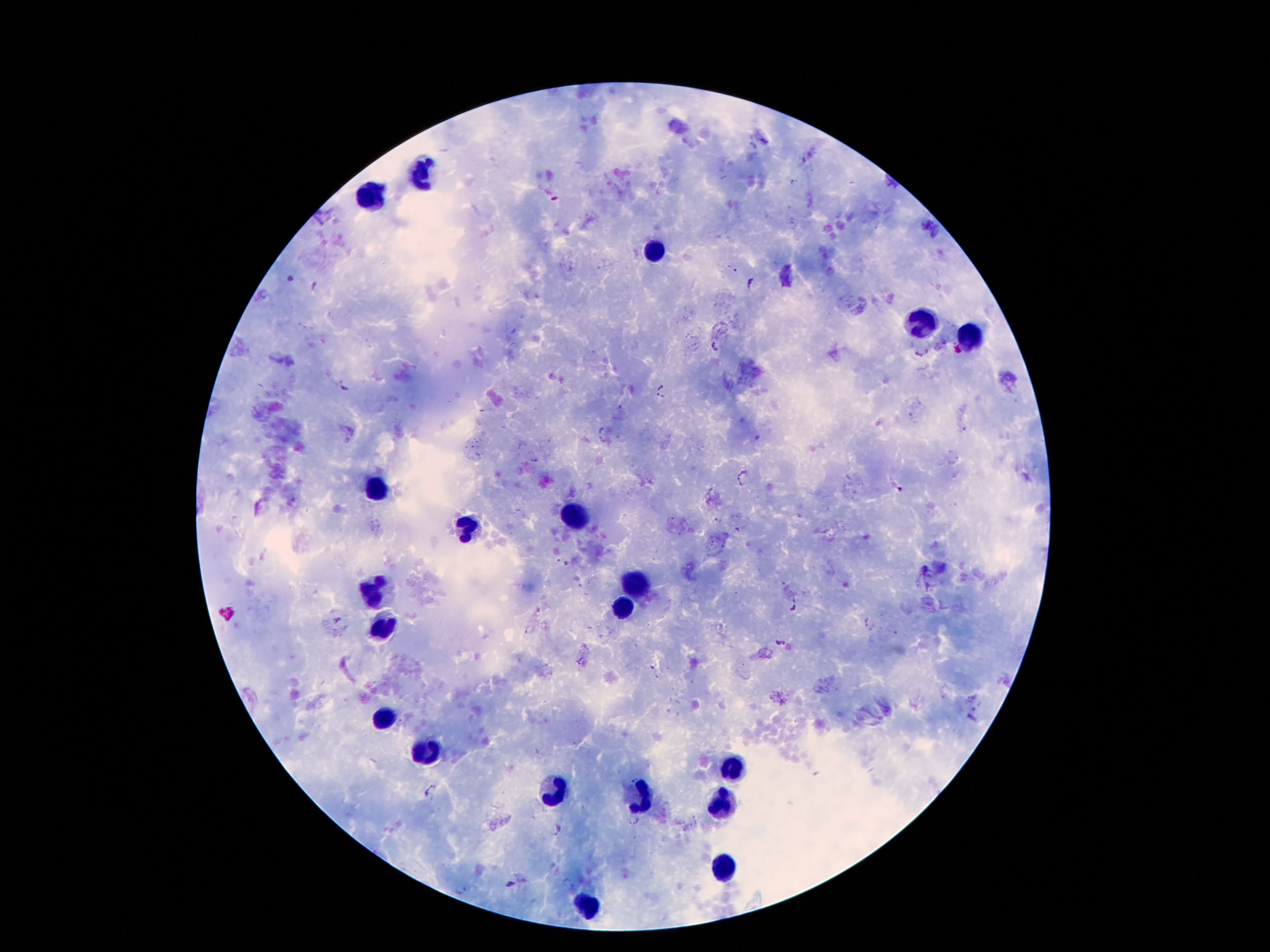

Approximate centers as (x, y) in pixels.
Summary:
  - Leukocyte locations: (420, 167), (372, 195), (659, 249), (922, 317), (973, 340), (377, 483), (575, 518), (463, 528), (634, 582), (372, 590), (629, 610), (382, 623), (382, 717), (425, 755), (733, 768), (550, 791), (639, 796), (718, 806), (723, 867), (588, 905)
  - Plasmodium parasite locations: (752, 281), (715, 347), (344, 386), (660, 389), (742, 478), (561, 561), (792, 606), (778, 644), (432, 789), (632, 824), (554, 830), (511, 884), (459, 888)
  - Preparation: thick peripheral-blood smear
  - Capture: smartphone through the microscope eyepiece
  - Patient malaria status: infected with Plasmodium falciparum
  - Stain: Giemsa
  - Magnification: 100x
  - Image size: 1270×952 pixels
  - Field of view: one from this slide